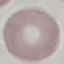
Summary:
  - Malaria status: uninfected
  - Stain: Giemsa
  - Capture: smartphone through the microscope eyepiece
  - Preparation: thin blood film
  - Image type: cell patch, automatically extracted from a larger field of view and resized to 64 × 64 pixels